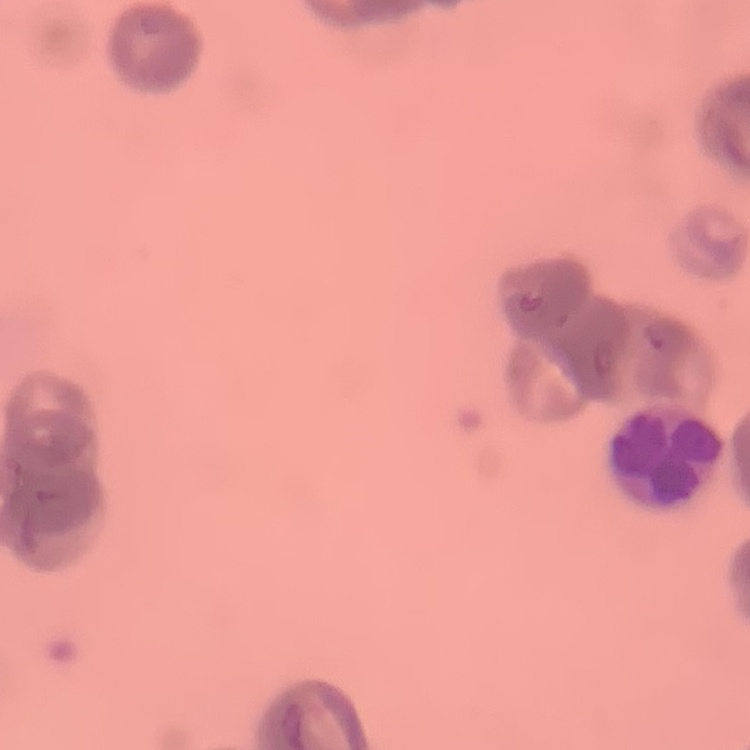

red_blood_cell_morphology: rouleaux formation
image_type: square crop of a larger photomicrograph
stain: Field's or Giemsa
preparation: thin blood film